Locate every Plasmodium parasite.
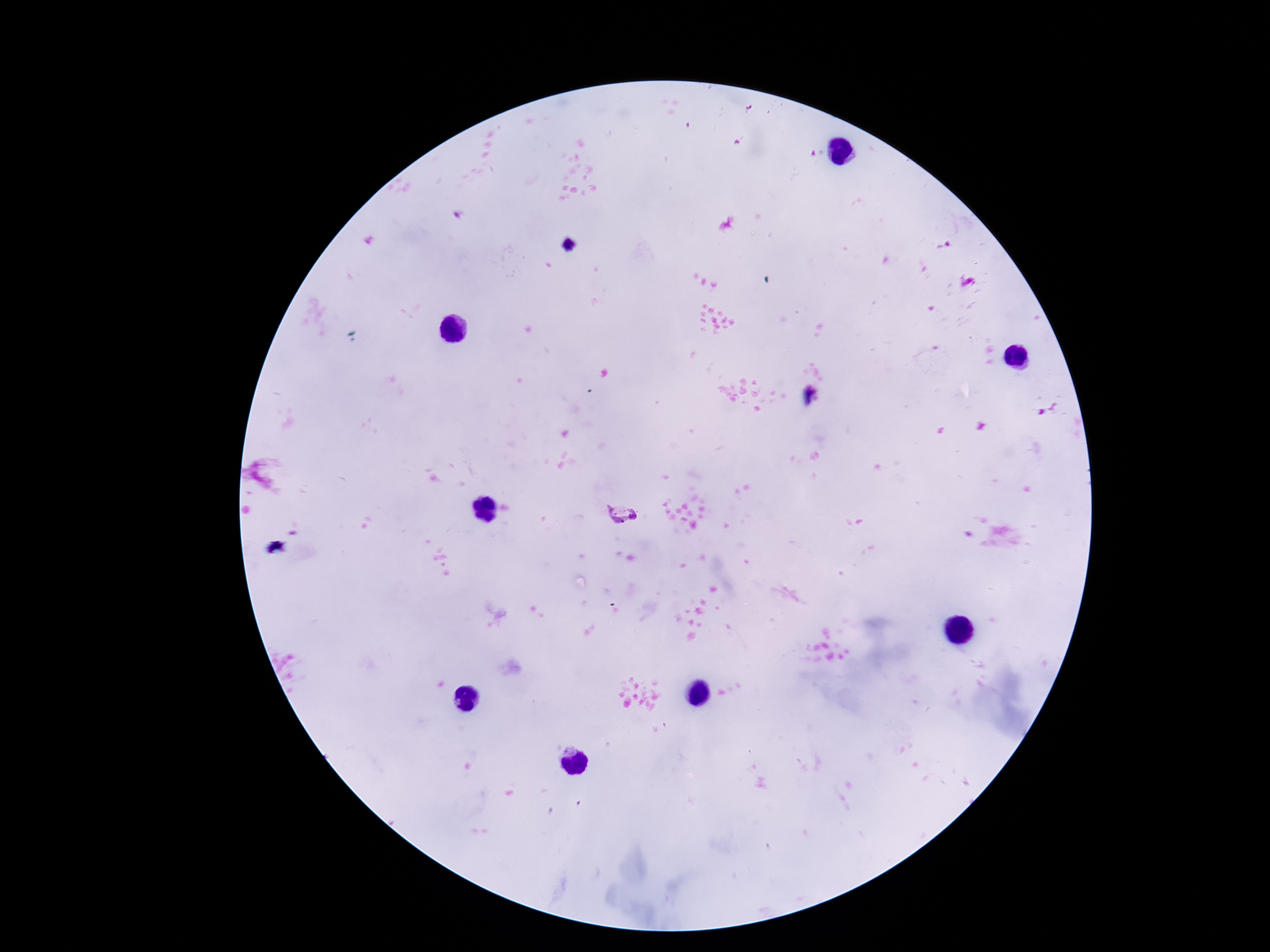

Approximate centers as (x, y) in pixels.
Plasmodium parasites: (622, 518).

Giemsa-stained preparation. Image is 1270×952 pixels. Thick peripheral-blood smear. One field from this slide. Smartphone photograph taken through the microscope eyepiece. Patient malaria status: positive. 100x magnification.